Comment on the morphology of the erythrocytes.
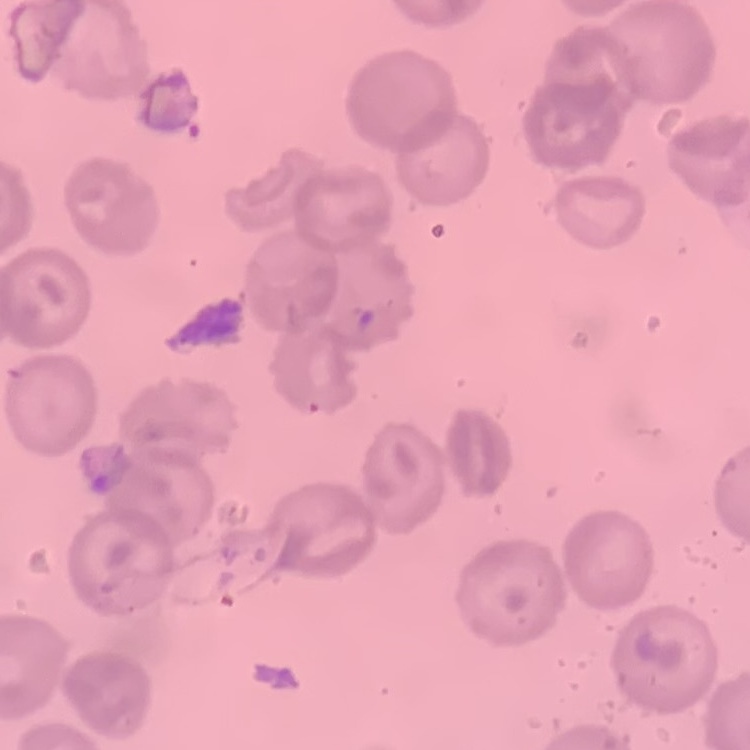
They show no rouleaux formation.

Summary:
  - Stain: Field's or Giemsa
  - Image type: one tile cut from a larger photomicrograph
  - Preparation: thin blood smear